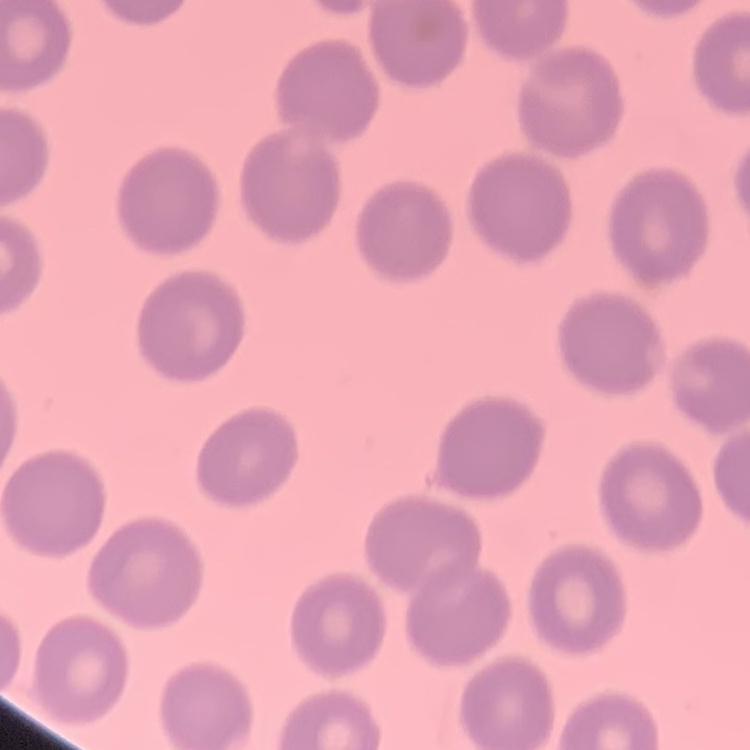

The red blood cells show no rouleaux formation. One tile cut from a larger photomicrograph. Stained with either Field's or Giemsa. Thin blood film.